Point out each leukocyte.
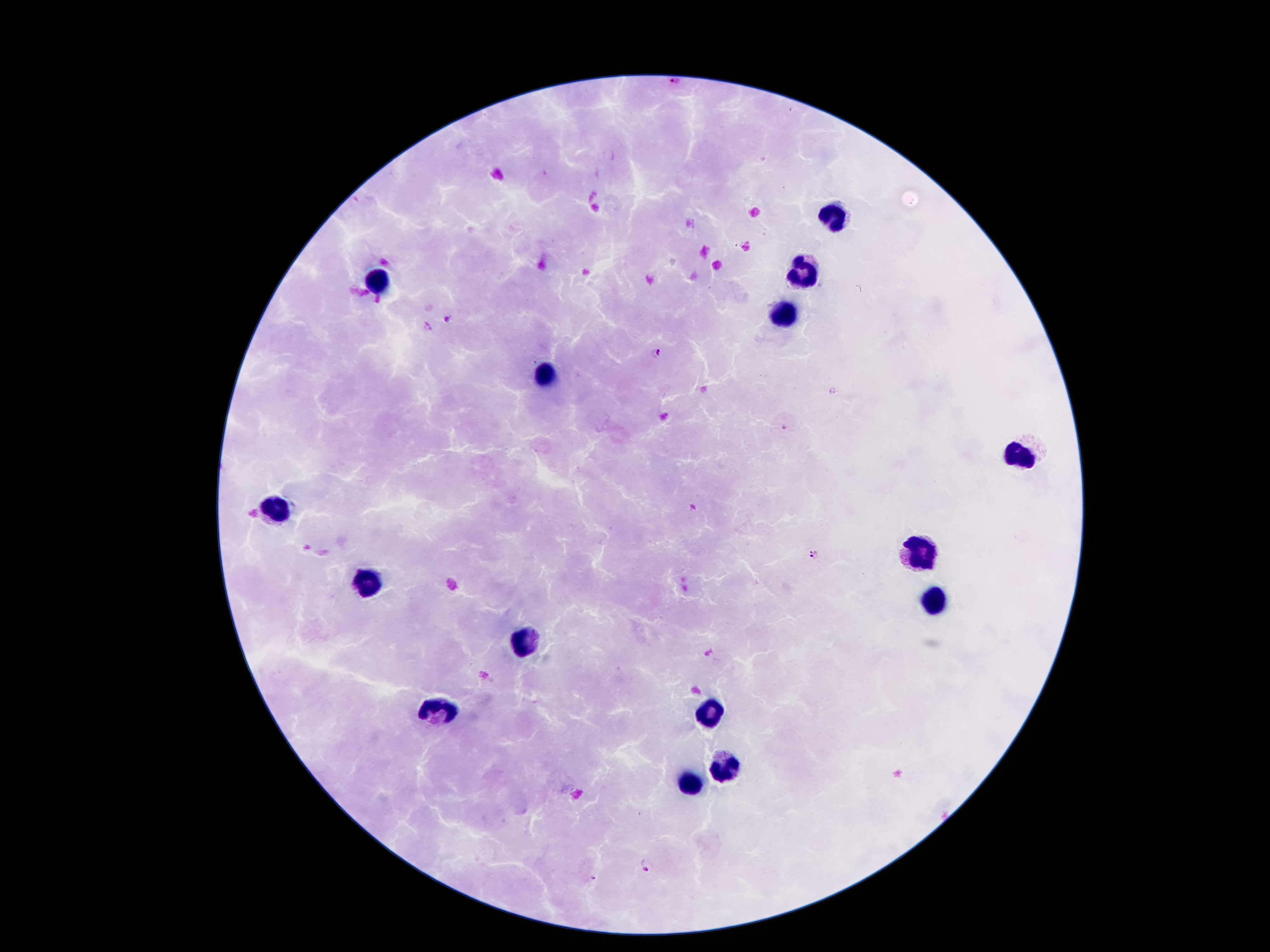
Approximate object centers, in pixels from the top-left corner.
Leukocytes: (x=833, y=215), (x=803, y=267), (x=381, y=279), (x=786, y=314), (x=544, y=375), (x=1021, y=457), (x=274, y=504), (x=917, y=553), (x=368, y=581), (x=937, y=603), (x=521, y=640), (x=435, y=709), (x=712, y=709), (x=719, y=763), (x=692, y=781).

Plasmodium parasite locations: (x=671, y=80), (x=448, y=319), (x=656, y=353), (x=785, y=429), (x=693, y=507), (x=811, y=554), (x=646, y=866), (x=593, y=879). Image is 1270×952 pixels. Thick peripheral-blood smear. Single field of view. Giemsa stain. Photographed through the microscope eyepiece with a smartphone camera. 100x magnification. Patient malaria status: positive for Plasmodium falciparum.